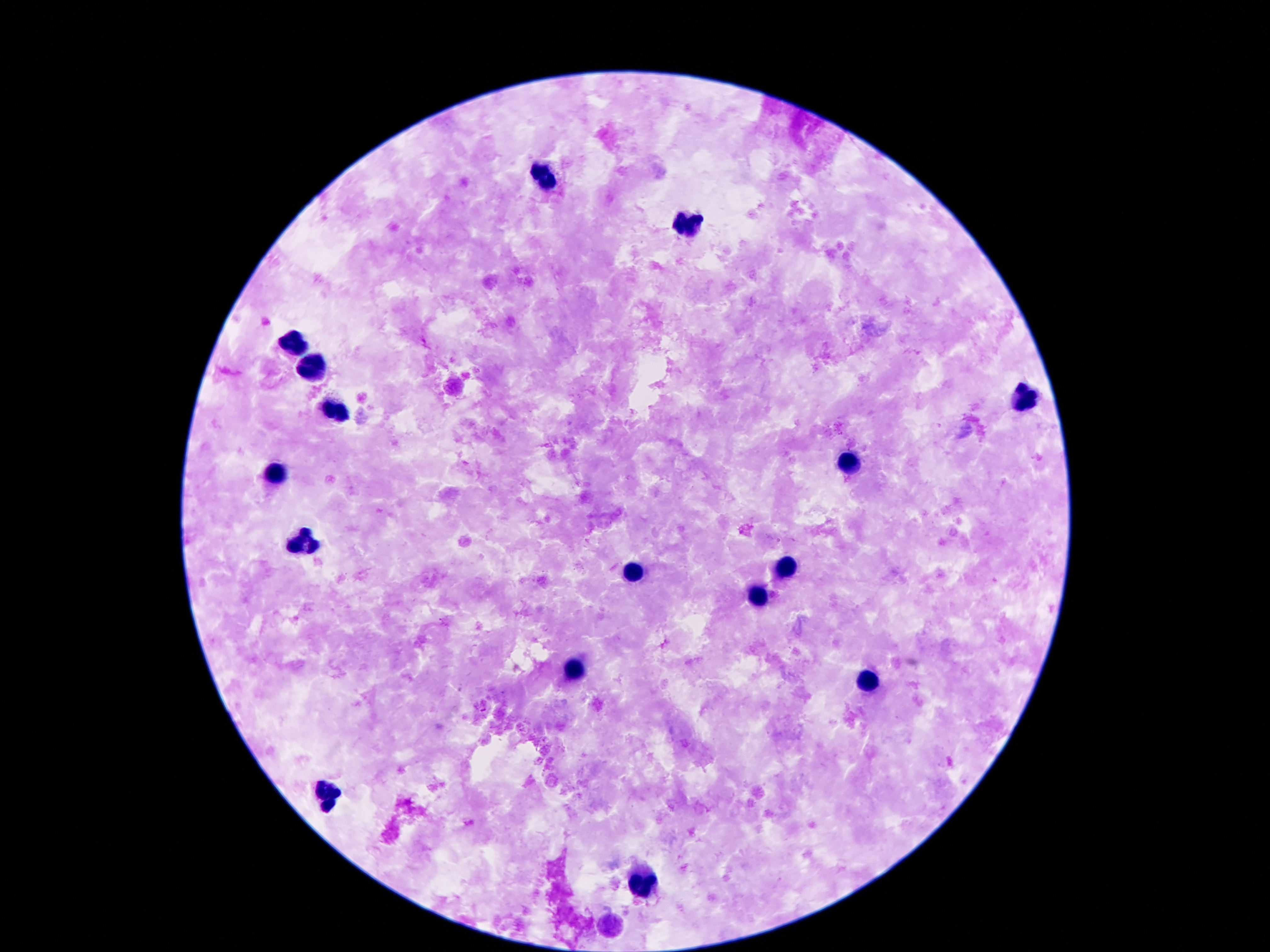
Approximate object centers, in pixels from the top-left corner.
Summary:
  - Leukocyte locations: (x=543, y=179), (x=689, y=227), (x=296, y=341), (x=316, y=365), (x=1024, y=400), (x=335, y=408), (x=851, y=462), (x=278, y=474), (x=296, y=545), (x=785, y=566), (x=634, y=576), (x=758, y=596), (x=573, y=672), (x=869, y=683), (x=328, y=796), (x=644, y=887)
  - Capture: smartphone camera through the microscope eyepiece
  - Patient malaria status: not infected
  - Field of view: single
  - Image size: 1270×952 pixels
  - Stain: Giemsa
  - Magnification: 100x
  - Preparation: thick peripheral-blood smear